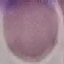

Summary:
  - Result: no malaria parasites seen
  - Image type: automatically extracted cell patch, resized to 64 × 64 pixels
  - Stain: Giemsa
  - Capture: smartphone through the microscope eyepiece
  - Preparation: thin blood film